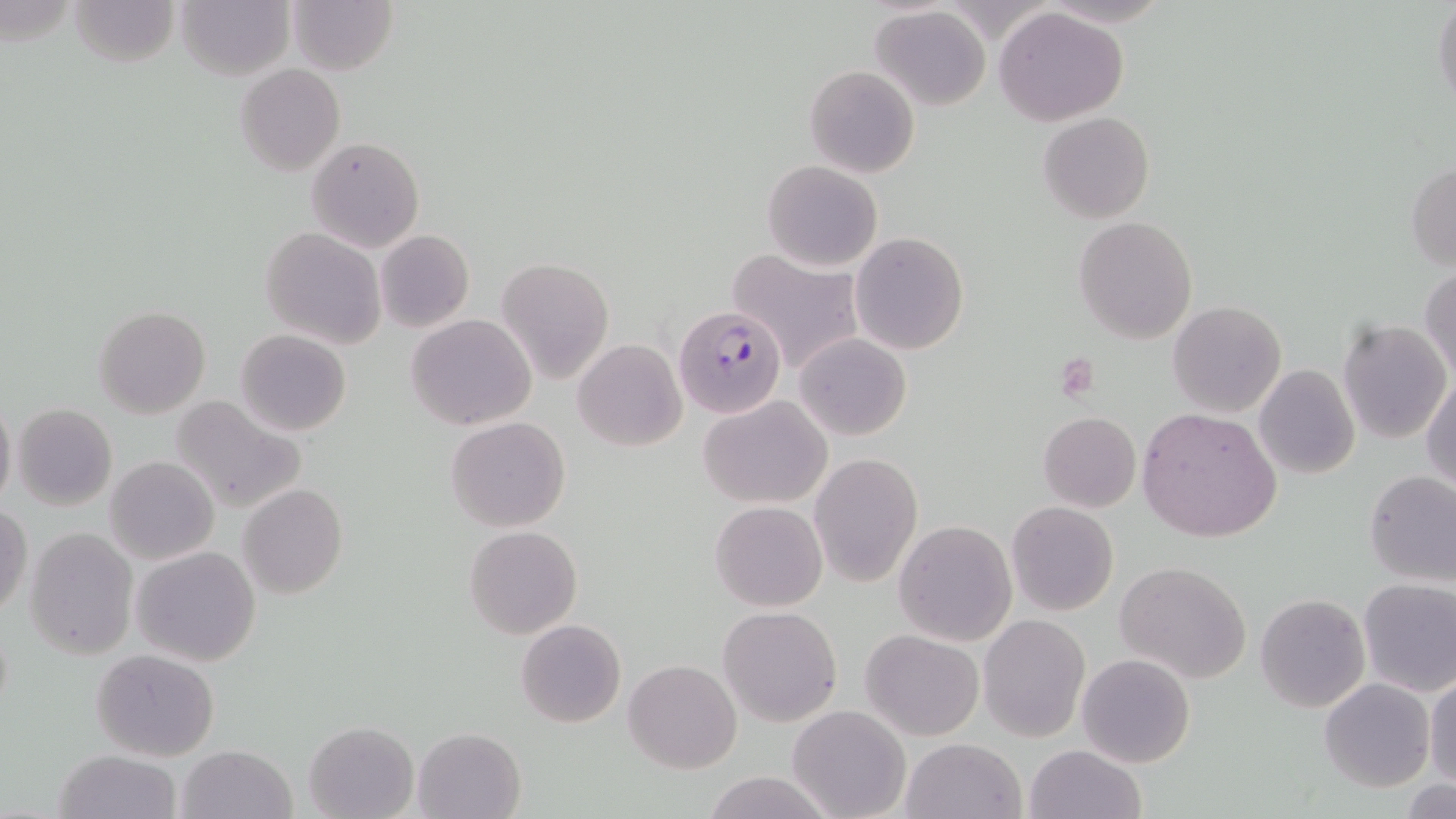
Summary:
  - Coordinate format: approximate bounding boxes as (x1,y1)-(x2,y2) corner pairs in pixels
  - Uninfected red blood cell locations: (68,0)-(179,69), (177,0)-(294,80), (287,0)-(397,75), (1432,0)-(1455,112), (870,7)-(990,111), (993,8)-(1130,127), (236,64)-(344,177), (805,65)-(920,179), (1039,112)-(1153,225), (307,136)-(424,253), (763,159)-(883,271), (1407,163)-(1455,270), (1074,217)-(1198,343), (260,228)-(386,350), (374,229)-(474,333), (850,232)-(969,355), (725,248)-(865,376), (496,258)-(614,385), (1420,264)-(1456,383), (1169,301)-(1288,418), (94,305)-(211,417), (405,312)-(537,431), (1338,319)-(1452,444), (235,329)-(352,438), (793,332)-(911,442), (573,339)-(686,452), (1254,364)-(1360,479), (1422,374)-(1455,493), (699,394)-(832,509), (169,395)-(305,514), (0,396)-(16,510), (13,403)-(117,510), (1136,406)-(1283,544), (1038,411)-(1140,511), (446,417)-(569,533), (809,452)-(923,588), (105,456)-(219,565), (1364,470)-(1456,588), (239,483)-(348,599), (711,501)-(826,612), (1007,502)-(1119,617), (0,505)-(31,617), (894,520)-(1017,645), (464,526)-(582,639), (25,527)-(139,662), (132,546)-(261,667), (1117,562)-(1252,683), (1358,579)-(1456,696), (1256,593)-(1369,712), (719,606)-(841,726), (978,613)-(1089,742), (516,619)-(626,727), (860,630)-(985,742), (824,644)-(948,775), (90,648)-(219,761), (1077,653)-(1194,767), (624,658)-(742,772), (1426,675)-(1456,787), (1319,677)-(1435,792), (788,703)-(911,819), (302,720)-(418,819), (413,727)-(526,819), (902,738)-(1025,819), (177,745)-(296,819), (1024,745)-(1145,819), (54,749)-(182,819), (701,771)-(841,819), (1404,779)-(1453,818)
  - Plasmodium falciparum-infected red blood cell locations: (674,305)-(788,418)
  - Platelet locations: (1056,355)-(1100,402)
  - Slide-level diagnosis: Plasmodium falciparum
  - Stain: May-Grünwald-Giemsa
  - Image size: 1456×819 pixels
  - Preparation: thin blood smear
  - Magnification: 1000x
  - Field of view: single
  - Modality: optical microscopy